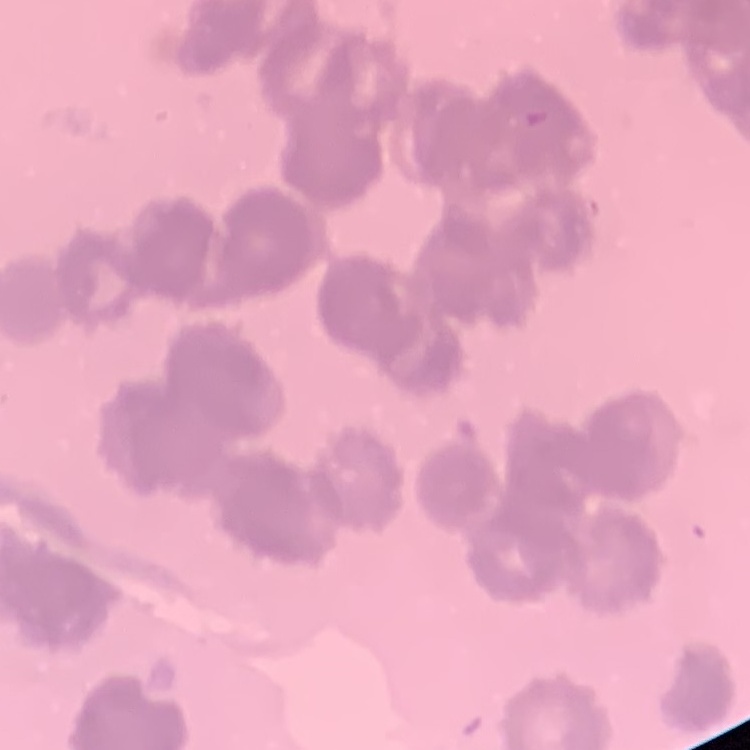

red blood cell morphology = rouleaux formation
preparation = thin blood film
stain = Field's or Giemsa
image type = one tile cut from a larger photomicrograph